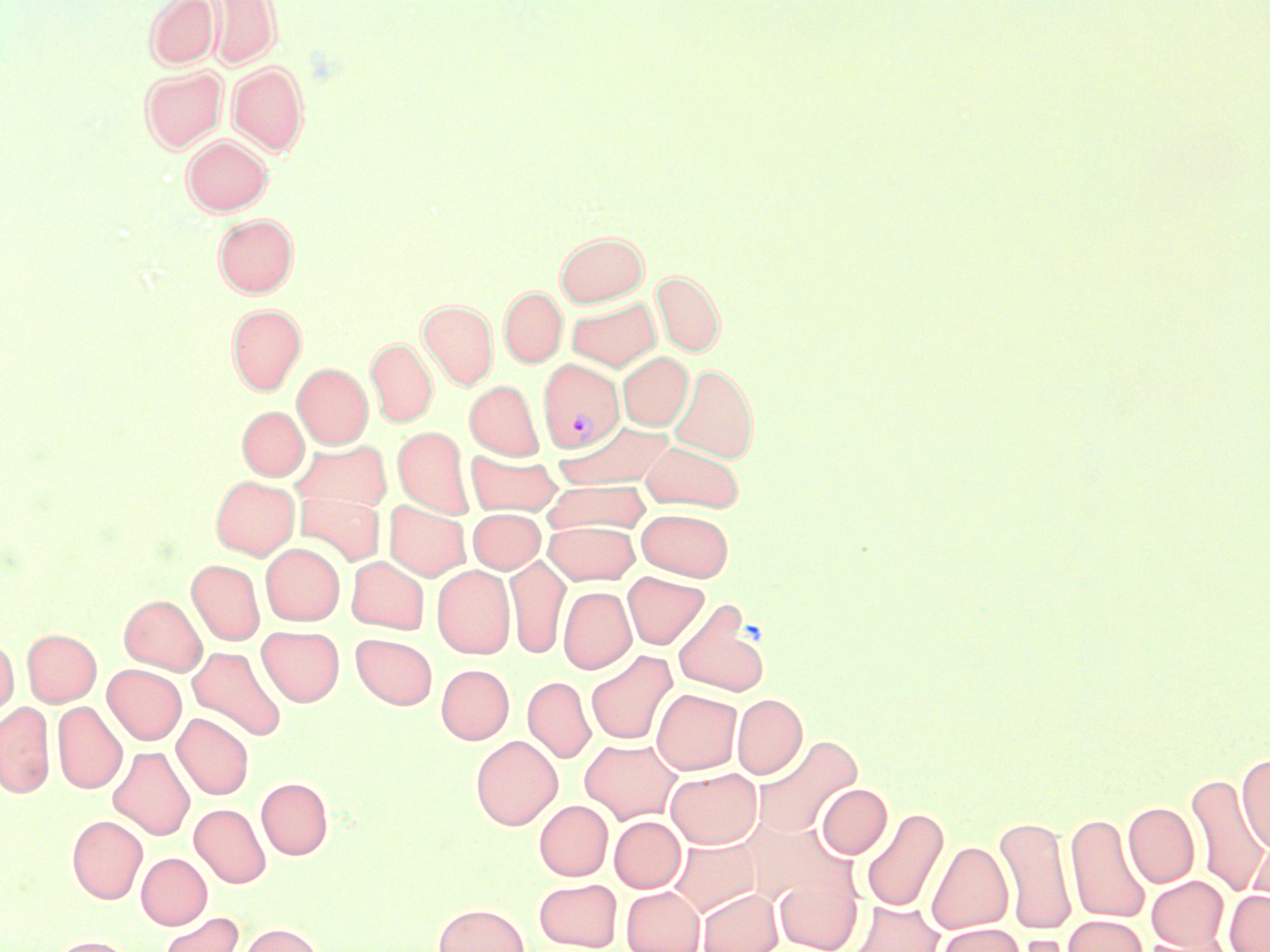 Approximate bounding boxes as [x1, y1, x2, y2] in pixels. Plasmodium vivax-infected red blood cell locations: [536, 358, 624, 455]. Uninfected red blood cell locations: [145, 0, 220, 69], [204, 1, 281, 69], [227, 62, 309, 155], [139, 65, 226, 152], [181, 134, 273, 215], [213, 214, 299, 297], [556, 230, 648, 307], [652, 270, 725, 355], [499, 286, 567, 367], [566, 296, 661, 371], [418, 300, 497, 389], [226, 304, 306, 394], [366, 337, 437, 427], [617, 352, 693, 430], [293, 363, 372, 448], [669, 363, 759, 462], [465, 380, 543, 459], [237, 406, 308, 480], [554, 421, 675, 490], [393, 427, 473, 517], [290, 439, 392, 513], [640, 440, 744, 512], [466, 451, 561, 516], [211, 476, 299, 559], [541, 479, 651, 536], [296, 492, 385, 565], [385, 501, 471, 580], [637, 508, 734, 580], [469, 509, 544, 573], [544, 521, 639, 585], [261, 543, 344, 625], [505, 555, 570, 658], [346, 556, 429, 633], [187, 559, 265, 645], [433, 565, 514, 659], [622, 571, 709, 649], [558, 586, 635, 674], [120, 594, 206, 674], [672, 601, 770, 697], [257, 625, 344, 706], [22, 629, 101, 706], [351, 633, 437, 709], [0, 636, 19, 717], [188, 646, 286, 741], [586, 651, 677, 745], [103, 664, 186, 744], [436, 664, 513, 744], [522, 676, 595, 763], [652, 689, 742, 775], [732, 693, 807, 778], [0, 701, 55, 797], [53, 702, 127, 793], [172, 713, 253, 799], [471, 735, 562, 829], [752, 735, 861, 838], [580, 738, 682, 823], [108, 746, 194, 840], [1236, 754, 1270, 854], [666, 768, 762, 849], [1185, 773, 1269, 897], [256, 777, 333, 859], [817, 784, 892, 858], [534, 800, 612, 880], [1123, 802, 1199, 887], [190, 803, 270, 888], [861, 807, 949, 913], [1065, 812, 1151, 924], [67, 815, 147, 903], [995, 815, 1076, 935], [610, 816, 685, 893], [746, 818, 853, 908], [669, 837, 761, 917], [1247, 838, 1270, 916], [927, 841, 1012, 933], [136, 853, 211, 929], [775, 871, 863, 951], [1148, 876, 1228, 950], [534, 878, 622, 950], [621, 886, 704, 952], [697, 888, 783, 952], [1225, 890, 1270, 952], [847, 900, 944, 952], [432, 903, 529, 952], [157, 912, 243, 952], [1064, 915, 1147, 952], [237, 922, 325, 952], [938, 923, 1025, 952], [1007, 934, 1073, 952], [1138, 934, 1231, 952], [47, 935, 136, 952]. Slide-level diagnosis: Plasmodium vivax. 1000x magnification. May-Grünwald-Giemsa-stained preparation. One field of a larger specimen. Image is 1270×952 pixels. Optical microscopy. Thin blood film.